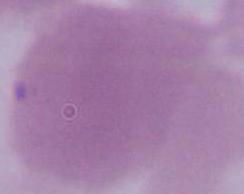 1000x magnification. An erythrocyte is seen. Micrograph.